Name the blood parasite species.
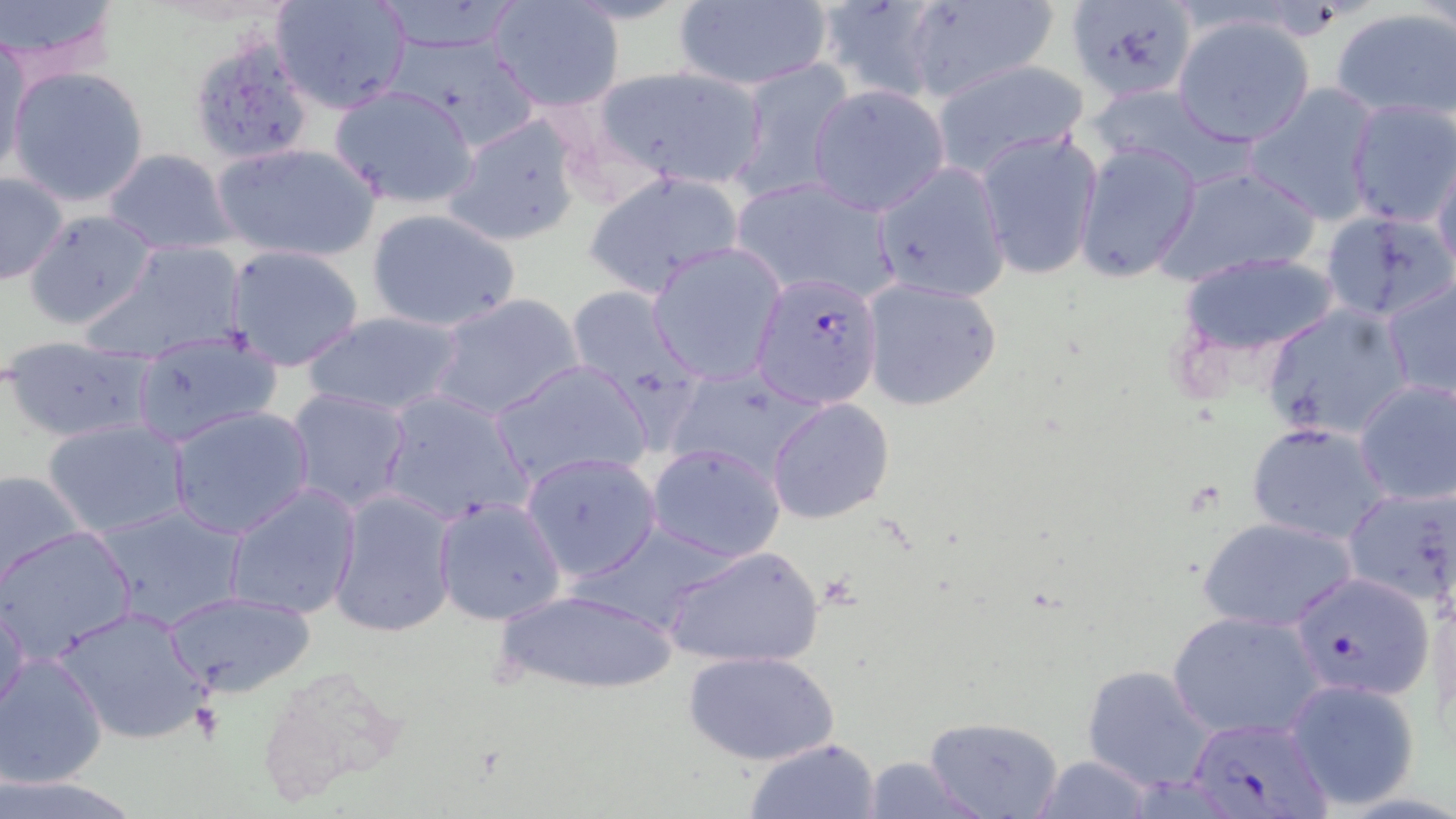

Plasmodium falciparum.

stain = May-Grünwald-Giemsa
modality = optical microscopy
field of view = single
image size = 1456×819 pixels
Plasmodium falciparum-infected red blood cell locations = approximate bounding boxes as [x1, y1, x2, y2] in pixels: [751, 272, 884, 407], [1288, 571, 1436, 702], [1186, 714, 1337, 818]
uninfected red blood cell locations = approximate bounding boxes as [x1, y1, x2, y2] in pixels: [1, 0, 123, 83], [814, 0, 950, 103], [1065, 0, 1198, 103], [270, 1, 413, 114], [486, 1, 624, 112], [671, 1, 833, 91], [899, 1, 1059, 103], [1330, 8, 1456, 122], [1172, 14, 1315, 147], [1, 34, 31, 180], [186, 34, 317, 167], [728, 57, 855, 202], [930, 59, 1090, 179], [7, 65, 151, 206], [589, 65, 773, 191], [1244, 82, 1380, 224], [806, 83, 951, 215], [328, 84, 480, 209], [1089, 85, 1243, 185], [1343, 99, 1456, 229], [444, 112, 586, 248], [976, 129, 1103, 279], [210, 141, 382, 264], [1074, 141, 1201, 283], [101, 149, 237, 255], [1431, 151, 1456, 278], [872, 162, 1011, 304], [1154, 164, 1323, 286], [583, 170, 746, 300], [0, 171, 70, 287], [729, 176, 902, 306], [365, 207, 521, 334], [24, 210, 160, 331], [1320, 211, 1454, 321], [86, 237, 252, 363], [648, 243, 785, 384], [223, 244, 367, 371], [1178, 251, 1343, 357], [1381, 275, 1456, 403], [861, 277, 1002, 410], [565, 286, 702, 408], [429, 292, 585, 423], [1262, 303, 1416, 443], [298, 310, 467, 419], [130, 332, 282, 445], [4, 338, 157, 444], [490, 359, 653, 490], [663, 366, 829, 485], [1352, 379, 1456, 506], [286, 388, 412, 513], [377, 390, 535, 526], [765, 397, 895, 524], [168, 405, 316, 540], [43, 418, 190, 538], [1245, 420, 1394, 544], [646, 443, 785, 562], [521, 451, 662, 581], [1, 469, 85, 590], [223, 481, 361, 622], [1341, 484, 1456, 609], [328, 491, 458, 638], [433, 497, 565, 626], [92, 504, 246, 630], [1199, 516, 1359, 633], [2, 526, 136, 664], [662, 543, 825, 669], [490, 587, 683, 695], [164, 591, 315, 695], [1, 595, 31, 720], [51, 604, 211, 746], [1166, 608, 1328, 741], [683, 649, 840, 765], [0, 653, 109, 788], [1082, 666, 1217, 793], [1283, 678, 1423, 809], [921, 715, 1066, 819], [742, 737, 883, 819], [1029, 754, 1160, 818], [856, 756, 992, 818]
platelet locations = approximate bounding boxes as [x1, y1, x2, y2] in pixels: [190, 701, 222, 740]
preparation = thin blood smear
magnification = 1000x